Name the blood parasite species.
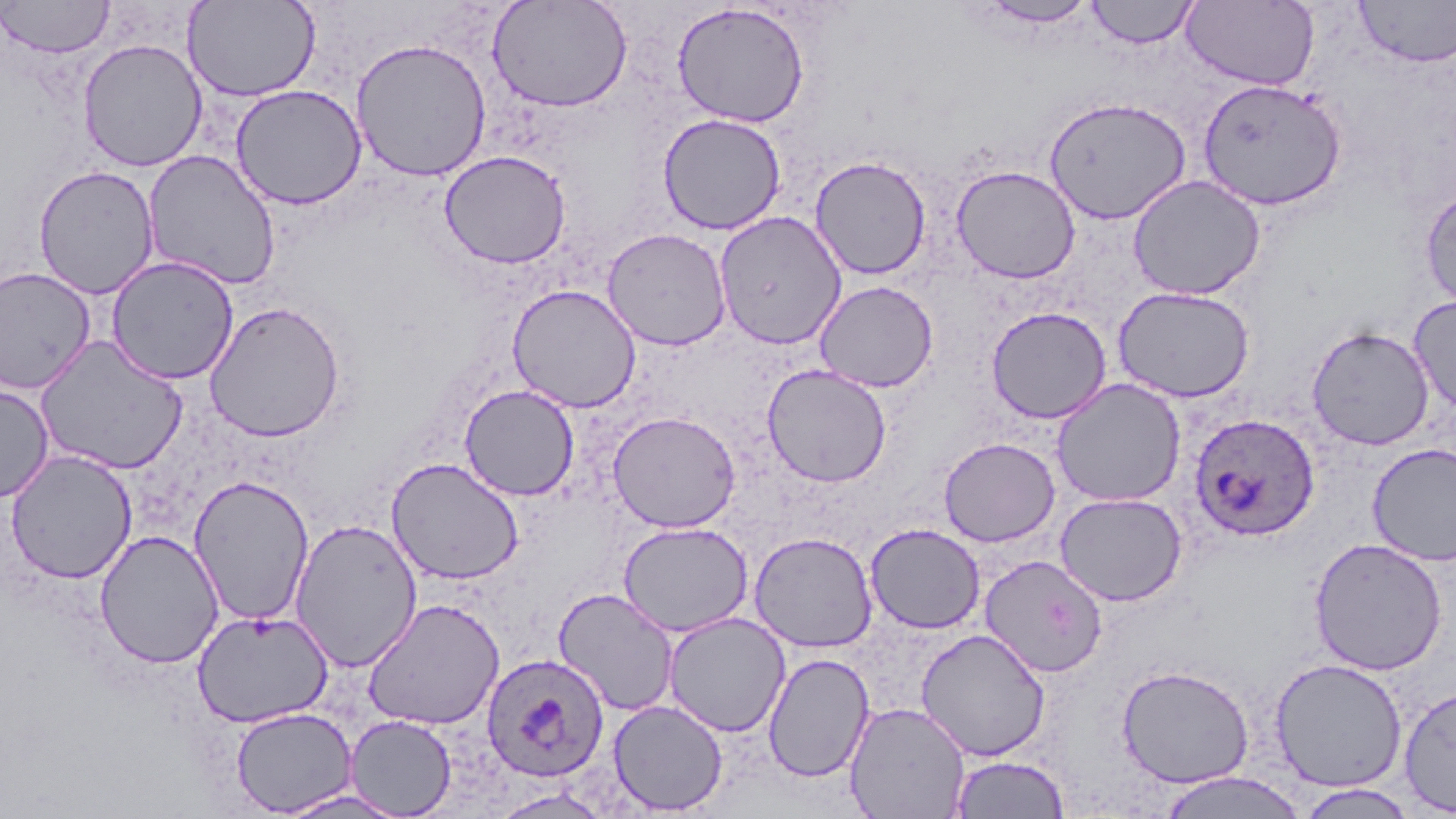

Plasmodium ovale.

{
  "preparation": "thin blood film",
  "stain": "May-Grünwald-Giemsa",
  "plasmodium_ovale_infected_red_blood_cell_locations": "approximate bounding boxes as (x1,y1)-(x2,y2) corner pairs in pixels: (1188,412)-(1321,541), (481,652)-(610,783)",
  "uninfected_red_blood_cell_locations": "approximate bounding boxes as (x1,y1)-(x2,y2) corner pairs in pixels: (1,0)-(114,58), (183,0)-(321,102), (976,0)-(1099,27), (1085,0)-(1200,48), (1182,0)-(1320,91), (1355,0)-(1456,68), (488,1)-(632,112), (672,2)-(809,127), (77,38)-(208,172), (350,38)-(492,181), (1197,78)-(1347,211), (230,84)-(367,210), (1044,96)-(1191,224), (657,113)-(786,235), (142,149)-(282,291), (439,150)-(571,269), (810,156)-(931,280), (32,165)-(160,299), (951,165)-(1081,283), (1127,175)-(1265,300), (1420,186)-(1456,313), (714,211)-(847,351), (602,227)-(732,350), (106,255)-(240,385), (0,267)-(97,395), (814,280)-(938,393), (507,284)-(641,413), (1113,286)-(1255,403), (1408,294)-(1456,415), (204,300)-(346,441), (987,306)-(1111,424), (1306,325)-(1435,451), (34,335)-(187,474), (762,364)-(891,487), (1051,378)-(1187,507), (0,381)-(54,504), (459,384)-(580,501), (607,410)-(741,532), (938,437)-(1060,547), (1367,443)-(1456,566), (5,449)-(138,584), (386,458)-(524,585), (187,474)-(315,626), (1055,492)-(1186,606), (289,518)-(423,672), (618,521)-(753,637), (865,523)-(985,633), (94,529)-(225,669), (749,532)-(878,652), (1308,537)-(1447,676), (979,554)-(1109,677), (553,587)-(679,716), (363,598)-(505,730), (192,609)-(334,728), (663,612)-(791,737), (915,629)-(1051,761), (762,652)-(874,783), (1269,657)-(1408,792), (1116,663)-(1255,788), (1398,684)-(1456,816), (607,699)-(728,815), (844,701)-(971,818), (230,707)-(357,816), (345,715)-(457,818), (949,754)-(1070,818), (1154,771)-(1310,819), (1295,784)-(1419,818), (272,788)-(408,818)",
  "modality": "light microscopy",
  "image_size": "1456×819 pixels",
  "magnification": "1000x",
  "field_of_view": "single"
}